State which cell type is depicted.
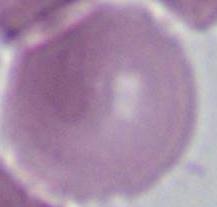
An erythrocyte.

Summary:
  - Magnification: 1000x
  - Modality: micrograph